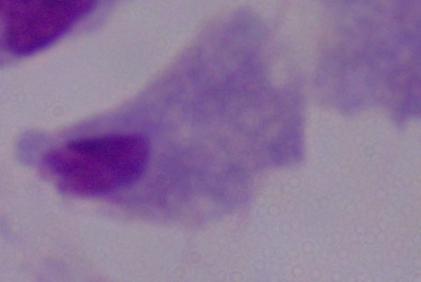

identification = trichomonad
modality = micrograph
magnification = 1000x